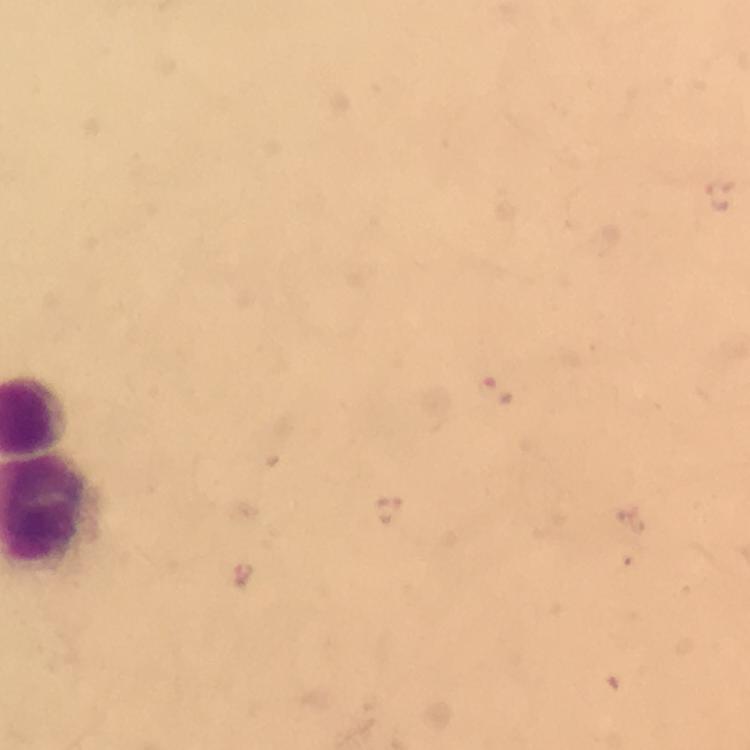 Approximate object centers, in pixels from the top-left corner. Malaria parasite locations: (x=721, y=194), (x=496, y=391), (x=390, y=510), (x=243, y=576). Thick blood film. Image is 750×750 pixels. Giemsa stain. From a diagnostic examination for malaria. A crop from one field of view. Immersion oil was used. At 100x magnification. Photographed through the microscope with a smartphone camera.